Identify the parasite.
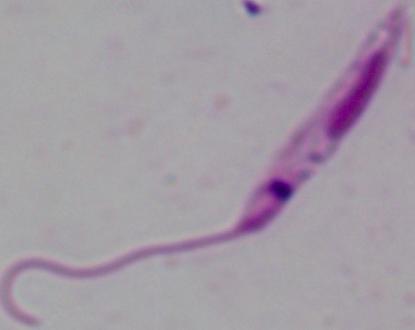

Leishmania.

modality = micrograph
magnification = 1000x